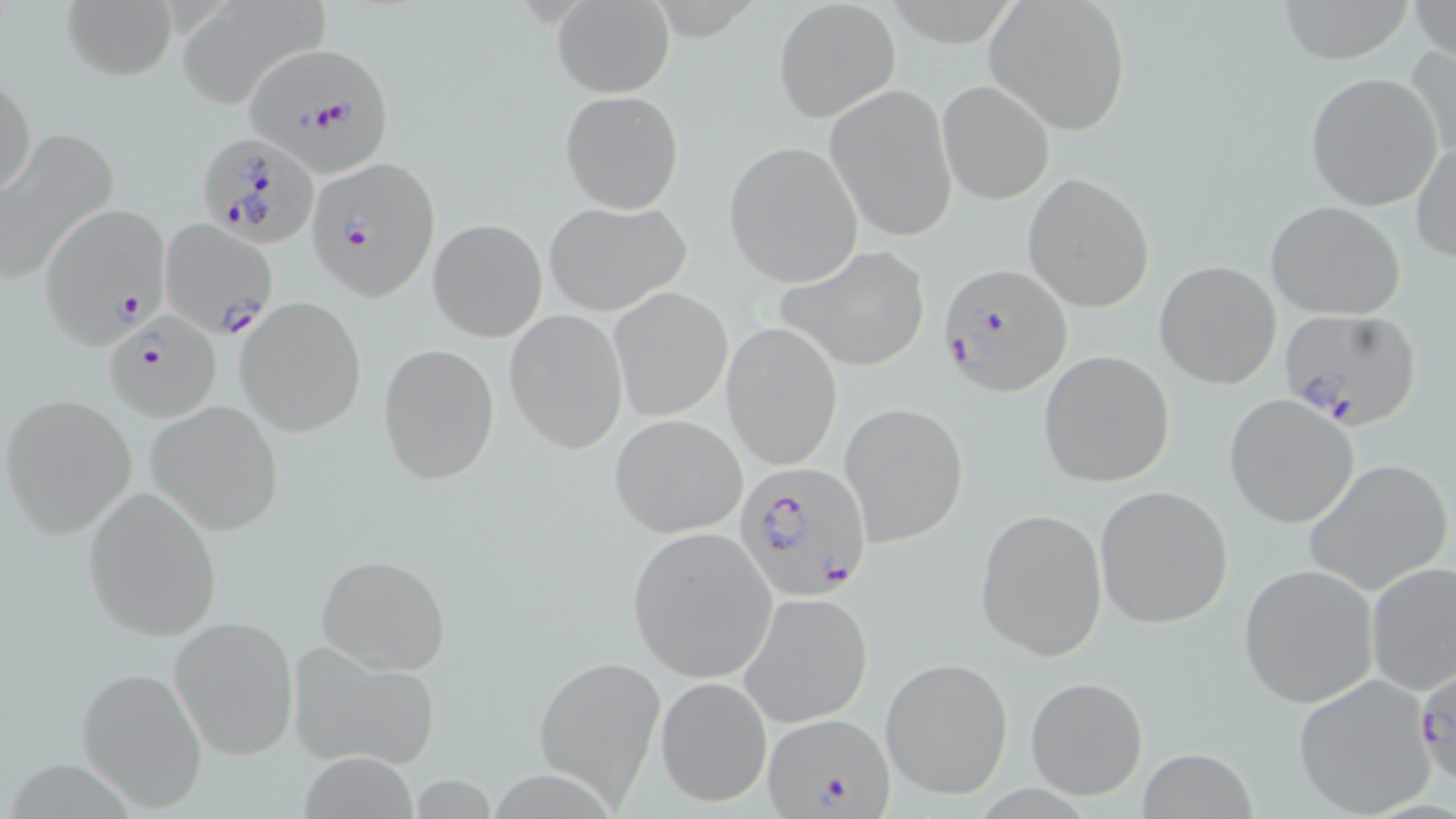

slide-level diagnosis = Plasmodium falciparum
magnification = 1000x
Plasmodium falciparum-infected red blood cell locations = approximate bounding boxes as [x1, y1, x2, y2] in pixels: [243, 40, 393, 185], [198, 131, 321, 247], [306, 155, 441, 299], [39, 200, 171, 347], [159, 219, 278, 337], [938, 263, 1071, 396], [1277, 306, 1424, 432], [104, 311, 223, 421], [738, 462, 871, 603], [762, 710, 896, 819]
preparation = thin blood smear
modality = light microscopy
image size = 1456×819 pixels
stain = May-Grünwald-Giemsa
field of view = one of a larger specimen
uninfected red blood cell locations = approximate bounding boxes as [x1, y1, x2, y2] in pixels: [63, 0, 176, 81], [987, 0, 1132, 133], [1270, 0, 1418, 63], [775, 1, 898, 121], [1408, 1, 1455, 64], [176, 3, 328, 105], [551, 3, 674, 95], [1406, 41, 1456, 163], [1, 66, 35, 203], [1304, 70, 1444, 211], [824, 81, 958, 243], [939, 81, 1054, 203], [560, 89, 683, 212], [0, 132, 114, 282], [1412, 139, 1455, 264], [723, 141, 863, 287], [1021, 173, 1156, 313], [542, 198, 691, 315], [1266, 201, 1406, 320], [428, 218, 547, 342], [778, 245, 934, 372], [1154, 260, 1282, 389], [610, 287, 733, 421], [235, 296, 367, 436], [505, 309, 629, 453], [723, 323, 843, 468], [377, 343, 500, 485], [1039, 349, 1176, 486], [1, 394, 139, 539], [1225, 395, 1358, 528], [145, 401, 284, 535], [840, 402, 968, 547], [610, 413, 747, 537], [1303, 458, 1452, 595], [1093, 485, 1234, 629], [82, 487, 224, 641], [975, 506, 1108, 662], [627, 526, 777, 681], [316, 554, 451, 675], [1365, 562, 1456, 700], [1239, 563, 1379, 708], [739, 593, 874, 727], [170, 616, 300, 759], [287, 638, 441, 770], [535, 654, 665, 803], [881, 657, 1014, 800], [76, 665, 207, 810], [1292, 675, 1437, 817], [655, 676, 772, 808], [1025, 676, 1146, 802], [1137, 749, 1259, 818], [296, 753, 418, 817]